Identify the cell.
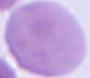
This is an erythrocyte.

Micrograph. Captured at 1000x magnification.